Assess the background quality.
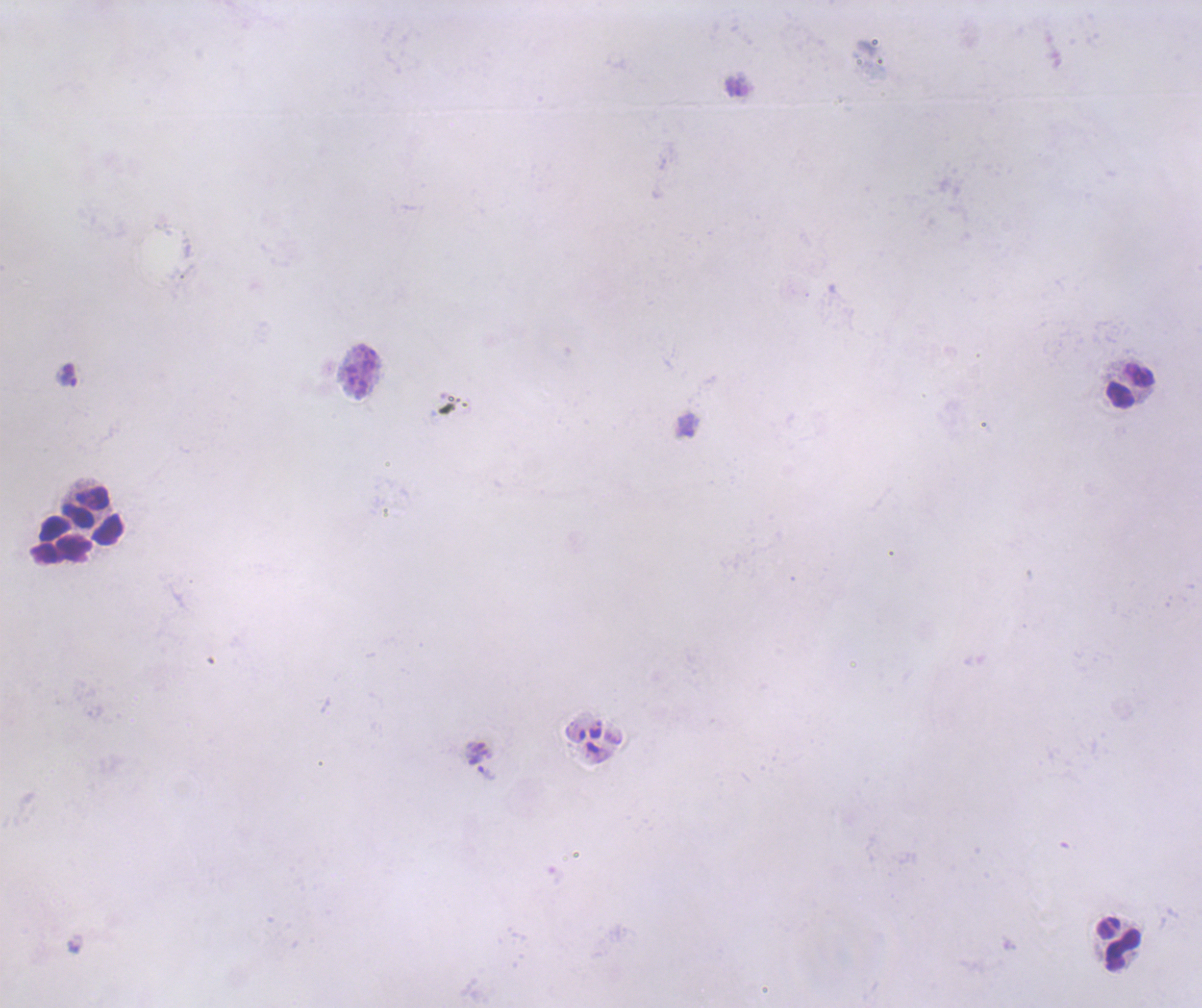
Poor.

Approximate object centers, in pixels from the top-left corner. Trophozoite locations: (x=68, y=376), (x=486, y=772). Leukocyte locations: (x=1130, y=387), (x=93, y=515), (x=59, y=538), (x=1118, y=944). 100x magnification. One field from this slide. Romanowsky stain. Coloration quality: bad. Thick blood smear. Previously used in an actual diagnosis. Image is 1202×1008 pixels. Result: Plasmodium parasites identified.